Report the malaria status of this cell.
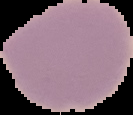

Uninfected.

Image is 133×115 pixels. Cell region segmented out of the field of view; the surrounding area is masked to black. From a thin blood smear.